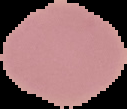 Image is 127×109 pixels. From a thin blood smear. Malaria status: uninfected. Cell region segmented out of the field of view; the surrounding area is masked to black.